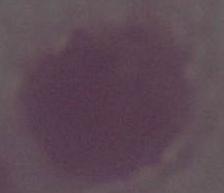
{
  "magnification": "1000x",
  "modality": "photomicrograph",
  "identification": "red blood cell"
}